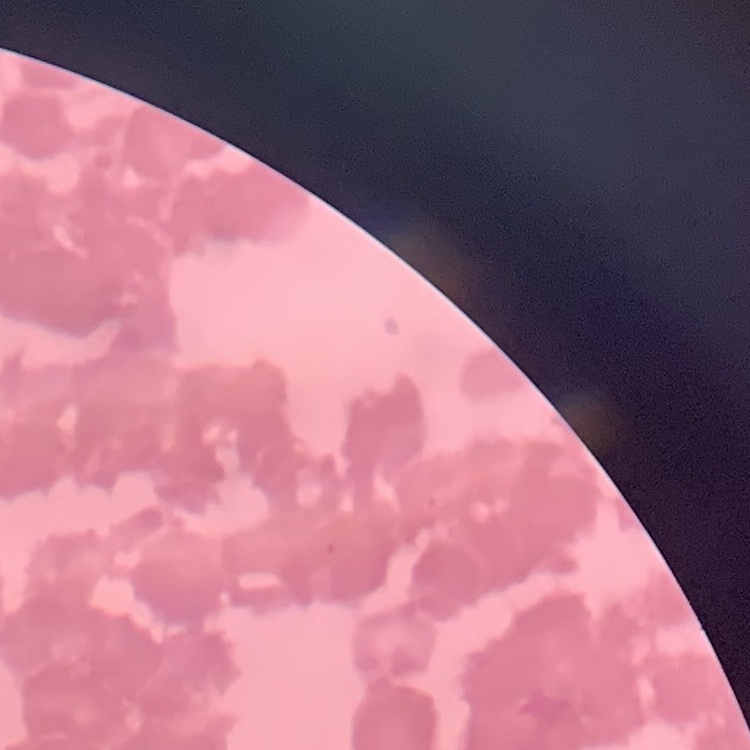
{
  "red_blood_cell_morphology": "rouleaux formation",
  "image_type": "one tile cut from a larger photomicrograph",
  "preparation": "thin peripheral smear",
  "stain": "Field's or Giemsa"
}